Identify the cell.
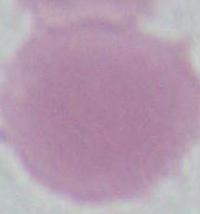

An erythrocyte.

Micrograph. Captured at 1000x magnification.